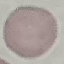

result = no malaria parasites seen
image type = automatically extracted cell patch, resized to 64 × 64 pixels
preparation = thin smear
capture = smartphone through the microscope eyepiece
stain = Giemsa